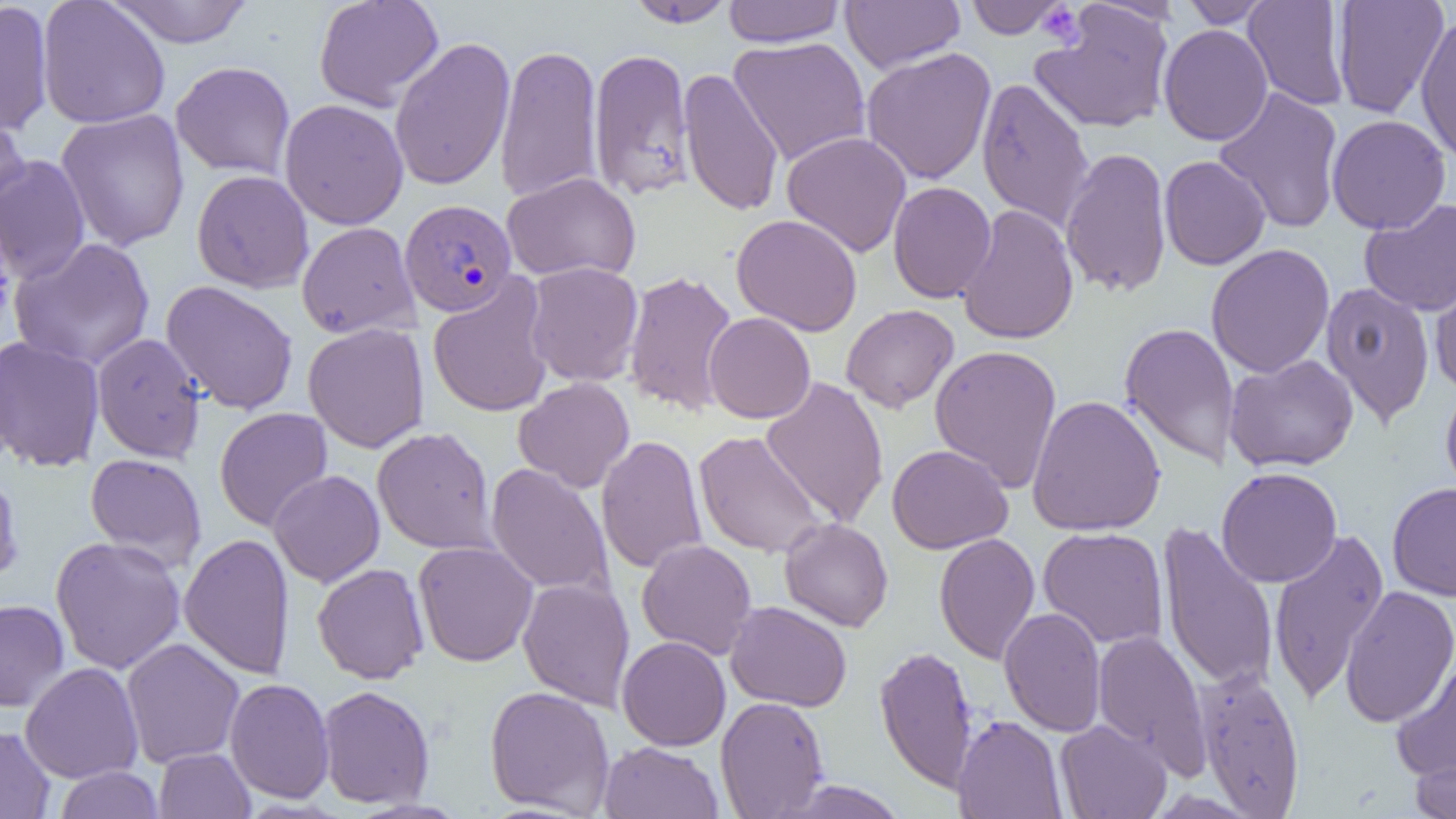

Approximate bounding boxes as (x1,y1)-(x2,y2) corner pairs in pixels. Platelet locations: (1037,3)-(1085,47). Uninfected red blood cell locations: (37,0)-(170,129), (104,0)-(254,47), (313,0)-(444,112), (625,0)-(736,28), (723,0)-(845,47), (965,0)-(1069,39), (1180,0)-(1274,28), (1243,0)-(1350,111), (1332,0)-(1449,118), (0,1)-(54,137), (841,1)-(964,74), (1030,2)-(1176,134), (1415,15)-(1456,164), (1158,24)-(1273,146), (389,36)-(515,192), (728,36)-(871,166), (494,42)-(603,205), (587,47)-(696,202), (860,47)-(997,185), (170,61)-(296,180), (678,67)-(784,217), (976,77)-(1095,231), (1213,87)-(1344,234), (279,98)-(409,230), (0,106)-(30,215), (55,109)-(190,251), (1326,114)-(1451,235), (781,131)-(912,258), (1060,147)-(1172,299), (0,155)-(91,284), (1159,155)-(1270,270), (191,169)-(314,293), (502,172)-(641,283), (888,181)-(996,303), (1359,198)-(1456,317), (957,204)-(1079,345), (731,214)-(863,336), (296,222)-(420,339), (9,237)-(155,372), (1205,243)-(1335,378), (524,261)-(644,387), (1429,263)-(1456,395), (623,269)-(739,417), (427,275)-(554,419), (160,280)-(299,415), (1319,281)-(1436,428), (841,304)-(959,413), (703,312)-(816,424), (1119,321)-(1240,471), (302,323)-(430,453), (91,332)-(207,463), (0,336)-(105,473), (930,344)-(1063,492), (1224,354)-(1359,472), (760,375)-(889,528), (513,377)-(635,493), (1440,382)-(1456,502), (1027,394)-(1166,536), (214,407)-(333,531), (372,426)-(498,555), (693,430)-(828,559), (595,435)-(708,575), (887,444)-(1013,553), (85,453)-(207,571), (485,463)-(614,597), (1216,466)-(1343,588), (0,467)-(23,588), (268,470)-(385,587), (1387,481)-(1456,601), (779,518)-(894,632), (1157,520)-(1279,693), (1038,527)-(1169,649), (1268,528)-(1389,705), (179,532)-(295,679), (933,533)-(1040,665), (50,535)-(186,674), (636,539)-(757,659), (413,541)-(539,667), (312,562)-(429,684), (517,577)-(635,711), (1339,585)-(1456,728), (0,599)-(69,712), (725,601)-(852,712), (999,606)-(1107,736), (1092,630)-(1210,774), (617,636)-(731,750), (121,638)-(245,769), (874,644)-(978,794), (1390,654)-(1456,786), (20,661)-(144,784), (1194,665)-(1306,818), (224,677)-(335,803), (317,685)-(435,809), (484,685)-(615,816), (715,696)-(830,818), (952,714)-(1067,819), (1055,720)-(1172,819), (0,725)-(56,819), (598,741)-(724,819), (1409,745)-(1456,819), (154,748)-(256,818), (55,766)-(164,817), (775,779)-(910,818), (345,798)-(471,818). Plasmodium vivax-infected red blood cell locations: (399,199)-(518,317). Slide-level diagnosis: Plasmodium vivax. Light microscopy. Thin blood film. Image is 1456×819 pixels. Single field of view. Captured at 1000x magnification.